Outline each blood parasite and name the species.
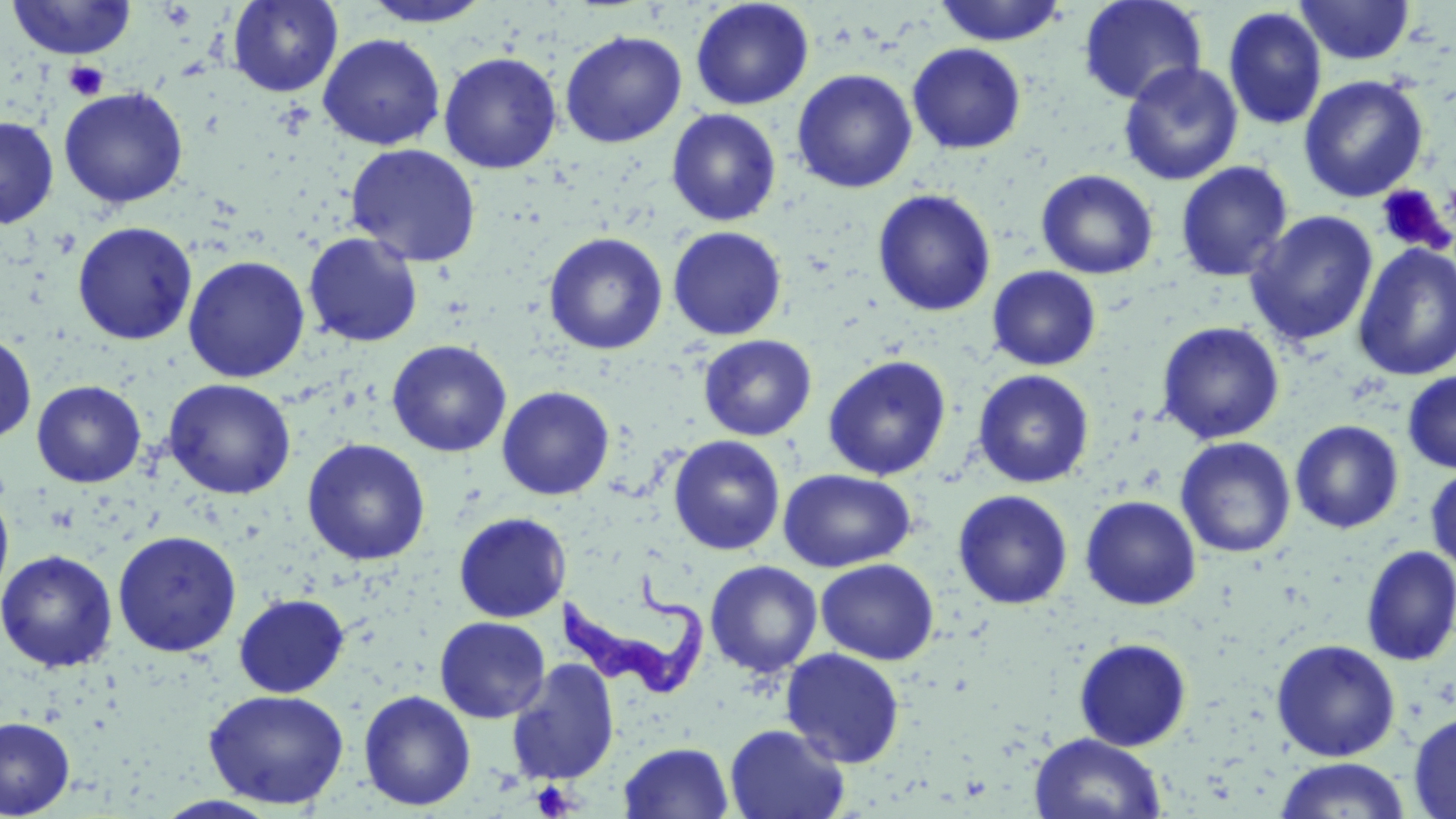
Approximate bounding boxes as named x1/y1/x2/y2 corners in pixels.
Trypanosoma brucei: (x1=555, y1=570, x2=708, y2=697).
No Plasmodium falciparum, Plasmodium ovale, Plasmodium malariae, Plasmodium vivax, or Babesia divergens observed.

Platelet locations: (x1=64, y1=60, x2=108, y2=101), (x1=1375, y1=185, x2=1453, y2=255), (x1=531, y1=781, x2=577, y2=819). Uninfected red blood cell locations: (x1=6, y1=0, x2=136, y2=60), (x1=228, y1=0, x2=342, y2=97), (x1=359, y1=0, x2=494, y2=28), (x1=933, y1=0, x2=1067, y2=46), (x1=1078, y1=0, x2=1207, y2=106), (x1=690, y1=1, x2=814, y2=110), (x1=1294, y1=1, x2=1414, y2=65), (x1=1223, y1=7, x2=1328, y2=130), (x1=560, y1=30, x2=687, y2=148), (x1=318, y1=34, x2=445, y2=151), (x1=907, y1=43, x2=1026, y2=154), (x1=438, y1=52, x2=562, y2=174), (x1=1118, y1=61, x2=1243, y2=186), (x1=792, y1=69, x2=917, y2=194), (x1=1299, y1=75, x2=1429, y2=202), (x1=58, y1=87, x2=189, y2=209), (x1=666, y1=108, x2=782, y2=226), (x1=0, y1=116, x2=59, y2=228), (x1=346, y1=143, x2=482, y2=267), (x1=1175, y1=161, x2=1293, y2=282), (x1=1036, y1=169, x2=1158, y2=279), (x1=872, y1=189, x2=996, y2=317), (x1=1244, y1=210, x2=1379, y2=347), (x1=72, y1=221, x2=197, y2=345), (x1=667, y1=226, x2=787, y2=340), (x1=303, y1=232, x2=423, y2=347), (x1=543, y1=232, x2=668, y2=355), (x1=1352, y1=243, x2=1456, y2=381), (x1=183, y1=256, x2=310, y2=383), (x1=987, y1=266, x2=1101, y2=371), (x1=1156, y1=321, x2=1285, y2=444), (x1=0, y1=333, x2=37, y2=444), (x1=698, y1=334, x2=816, y2=441), (x1=386, y1=339, x2=512, y2=457), (x1=822, y1=354, x2=952, y2=481), (x1=973, y1=369, x2=1094, y2=488), (x1=1402, y1=370, x2=1456, y2=474), (x1=163, y1=378, x2=296, y2=499), (x1=31, y1=380, x2=146, y2=487), (x1=497, y1=386, x2=614, y2=500), (x1=1289, y1=420, x2=1404, y2=534), (x1=668, y1=435, x2=786, y2=556), (x1=1175, y1=436, x2=1296, y2=558), (x1=302, y1=438, x2=430, y2=566), (x1=1425, y1=466, x2=1456, y2=573), (x1=778, y1=469, x2=916, y2=571), (x1=0, y1=490, x2=14, y2=603), (x1=953, y1=490, x2=1073, y2=609), (x1=1080, y1=495, x2=1201, y2=610), (x1=453, y1=511, x2=570, y2=622), (x1=112, y1=530, x2=242, y2=657), (x1=1359, y1=545, x2=1456, y2=667), (x1=0, y1=550, x2=117, y2=672), (x1=816, y1=559, x2=939, y2=665), (x1=704, y1=560, x2=822, y2=678), (x1=233, y1=594, x2=349, y2=697), (x1=434, y1=616, x2=551, y2=723), (x1=1074, y1=638, x2=1192, y2=751), (x1=1271, y1=639, x2=1401, y2=762), (x1=781, y1=648, x2=905, y2=768), (x1=505, y1=658, x2=620, y2=786), (x1=204, y1=689, x2=349, y2=809), (x1=358, y1=690, x2=476, y2=811), (x1=1408, y1=711, x2=1456, y2=819), (x1=1, y1=716, x2=75, y2=818), (x1=724, y1=724, x2=850, y2=819), (x1=1029, y1=733, x2=1167, y2=819), (x1=618, y1=741, x2=734, y2=819), (x1=1273, y1=757, x2=1411, y2=818), (x1=153, y1=795, x2=282, y2=818). Slide-level diagnosis: Trypanosoma brucei. Image is 1456×819 pixels. Optical microscopy. 1000x magnification. May-Grünwald-Giemsa-stained preparation. Thin blood film. Single field of view.